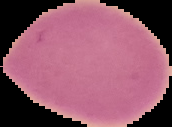
Image is 172×127 pixels. From a thin blood smear. Result: negative for Plasmodium parasites. Cell region segmented out of the field of view; the surrounding area is masked to black.